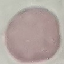

Summary:
  - Result: negative for malaria parasites
  - Image type: automatically extracted cell patch, resized to 64 × 64 pixels
  - Preparation: thin smear
  - Capture: smartphone camera at the microscope eyepiece
  - Stain: Giemsa